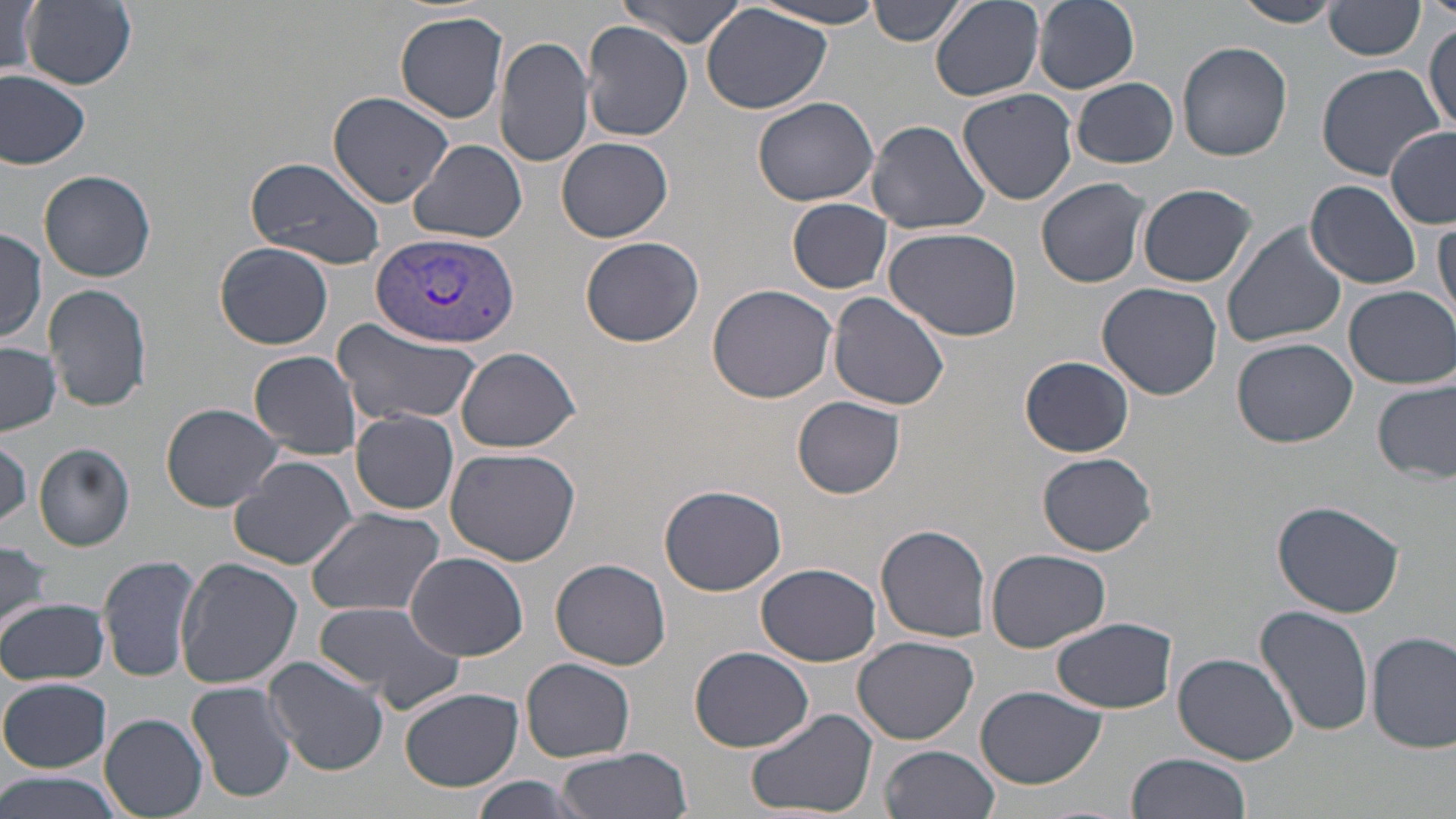

Summary:
  - Coordinate format: approximate bounding boxes as (x1,y1)-(x2,y2) corner pairs in pixels
  - Plasmodium vivax-infected red blood cell locations: (370,231)-(520,350)
  - Uninfected red blood cell locations: (20,0)-(137,89), (867,0)-(965,49), (929,0)-(1045,102), (1033,0)-(1139,92), (1231,0)-(1339,28), (614,2)-(752,47), (750,2)-(890,30), (3,3)-(43,80), (1324,3)-(1425,61), (701,4)-(833,116), (394,11)-(509,124), (1425,17)-(1455,135), (582,24)-(693,140), (494,34)-(595,171), (1177,41)-(1294,161), (1314,62)-(1445,180), (1,70)-(93,167), (1074,78)-(1179,168), (957,88)-(1079,206), (327,90)-(454,207), (752,96)-(879,206), (866,119)-(991,235), (1385,127)-(1456,228), (556,136)-(674,242), (408,139)-(527,243), (246,155)-(386,270), (39,171)-(156,283), (1036,177)-(1153,288), (1305,180)-(1424,288), (1138,184)-(1258,288), (787,198)-(892,293), (1433,220)-(1455,325), (1222,223)-(1347,352), (883,225)-(1025,345), (0,229)-(48,344), (580,235)-(704,347), (214,242)-(334,349), (1096,281)-(1222,400), (45,283)-(151,412), (707,284)-(839,403), (1345,285)-(1455,387), (825,291)-(951,411), (331,319)-(483,428), (1232,337)-(1357,447), (1,341)-(61,435), (455,346)-(581,454), (249,350)-(365,459), (1020,356)-(1135,457), (1373,380)-(1456,484), (793,396)-(905,498), (161,402)-(284,511), (349,409)-(459,516), (0,437)-(31,529), (33,441)-(136,552), (445,447)-(582,567), (1037,452)-(1156,557), (229,455)-(358,570), (659,483)-(788,596), (1272,498)-(1406,618), (304,506)-(445,618), (875,524)-(993,642), (0,540)-(53,637), (986,548)-(1112,654), (404,551)-(531,660), (99,552)-(203,683), (177,557)-(303,689), (552,558)-(673,672), (758,562)-(880,666), (1,597)-(109,685), (311,601)-(466,714), (1253,606)-(1374,737), (1051,618)-(1178,713), (1368,631)-(1455,753), (852,636)-(978,744), (690,646)-(814,753), (1173,652)-(1299,765), (263,656)-(390,775), (522,657)-(635,762), (1,677)-(111,773), (188,679)-(298,804), (976,686)-(1107,789), (400,687)-(523,791), (742,705)-(878,819), (99,714)-(208,818), (881,744)-(1000,819), (554,749)-(690,819), (1125,753)-(1252,819), (0,771)-(125,819), (471,775)-(586,817)
  - Slide-level diagnosis: Plasmodium vivax
  - Stain: May-Grünwald-Giemsa
  - Field of view: single
  - Magnification: 1000x
  - Modality: light microscopy
  - Image size: 1456×819 pixels
  - Preparation: thin blood smear